Identify the parasite.
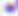
Toxoplasma gondii.

magnification = 400x
modality = photomicrograph